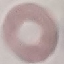

Summary:
  - Malaria status: uninfected
  - Preparation: thin smear
  - Image type: cell patch, automatically extracted from a larger field of view and resized to 64 × 64 pixels
  - Capture: smartphone through the microscope eyepiece
  - Stain: Giemsa